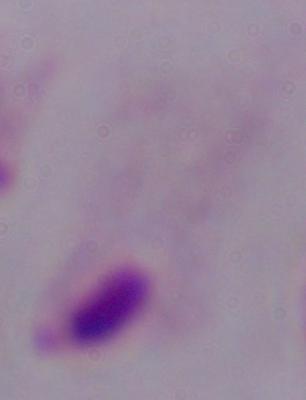

Micrograph. 1000x magnification. A trichomonad is shown.